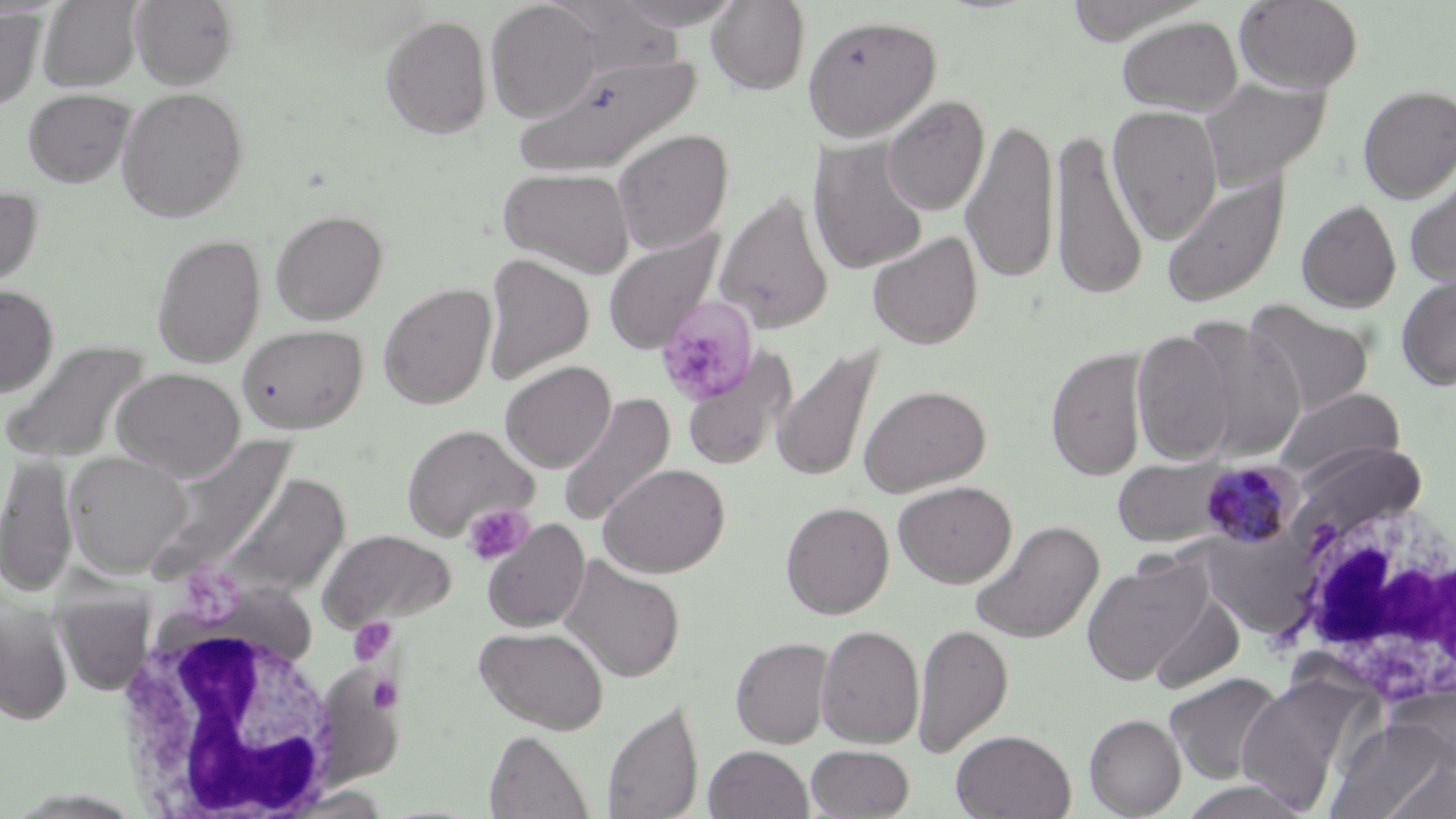
Approximate bounding boxes as (x1, y1, x2, y2) in pixels. White blood cell locations: (1284, 488, 1456, 711), (110, 586, 344, 816). Plasmodium malariae-infected red blood cell locations: (1198, 459, 1302, 550). Uninfected red blood cell locations: (39, 0, 142, 92), (131, 0, 239, 88), (607, 0, 746, 30), (1234, 0, 1364, 93), (485, 1, 603, 122), (705, 1, 810, 95), (544, 3, 687, 78), (0, 7, 45, 111), (379, 14, 492, 139), (803, 15, 941, 140), (1116, 15, 1243, 115), (513, 53, 703, 177), (1198, 76, 1330, 192), (1357, 83, 1456, 202), (116, 87, 248, 223), (23, 88, 136, 188), (882, 95, 990, 216), (1108, 105, 1225, 244), (962, 116, 1058, 286), (612, 128, 734, 253), (1050, 128, 1148, 302), (809, 139, 929, 276), (498, 166, 635, 277), (1404, 170, 1456, 289), (1161, 172, 1289, 308), (0, 185, 43, 294), (715, 191, 834, 335), (1296, 199, 1402, 312), (270, 209, 389, 324), (603, 229, 725, 354), (868, 231, 983, 349), (151, 232, 267, 367), (482, 254, 595, 383), (1396, 272, 1456, 390), (378, 282, 497, 409), (0, 285, 59, 398), (1245, 300, 1375, 415), (1183, 321, 1306, 462), (238, 324, 368, 434), (1132, 327, 1239, 466), (1, 340, 152, 463), (772, 343, 882, 484), (1046, 346, 1150, 480), (682, 348, 797, 472), (500, 360, 616, 472), (112, 366, 245, 479), (859, 383, 991, 497), (1274, 387, 1404, 481), (557, 393, 676, 526), (403, 423, 539, 541), (152, 437, 295, 573), (65, 451, 192, 576), (0, 453, 77, 597), (1111, 457, 1236, 547), (598, 462, 730, 578), (217, 471, 350, 599), (892, 480, 1017, 587), (780, 501, 894, 619), (482, 518, 590, 633), (968, 520, 1104, 645), (320, 529, 457, 627), (559, 556, 685, 683), (1082, 556, 1213, 686), (53, 592, 155, 695), (1146, 592, 1245, 695), (1, 598, 74, 724), (912, 623, 1013, 758), (816, 624, 924, 748), (474, 626, 610, 734), (731, 637, 834, 748), (1164, 672, 1284, 785), (1236, 676, 1359, 811), (601, 699, 704, 819), (1084, 713, 1186, 817), (1326, 719, 1450, 819), (951, 729, 1077, 819), (484, 730, 594, 818), (704, 745, 814, 819), (805, 745, 914, 818), (1380, 756, 1456, 819), (1174, 780, 1319, 819). Platelet locations: (654, 296, 759, 406), (462, 503, 534, 565), (184, 569, 247, 632), (349, 617, 395, 664), (365, 675, 402, 712). Slide-level diagnosis: Plasmodium malariae. Thin blood smear. One field of a larger specimen. May-Grünwald-Giemsa-stained preparation. 1000x magnification. Light microscopy. Image is 1456×819 pixels.